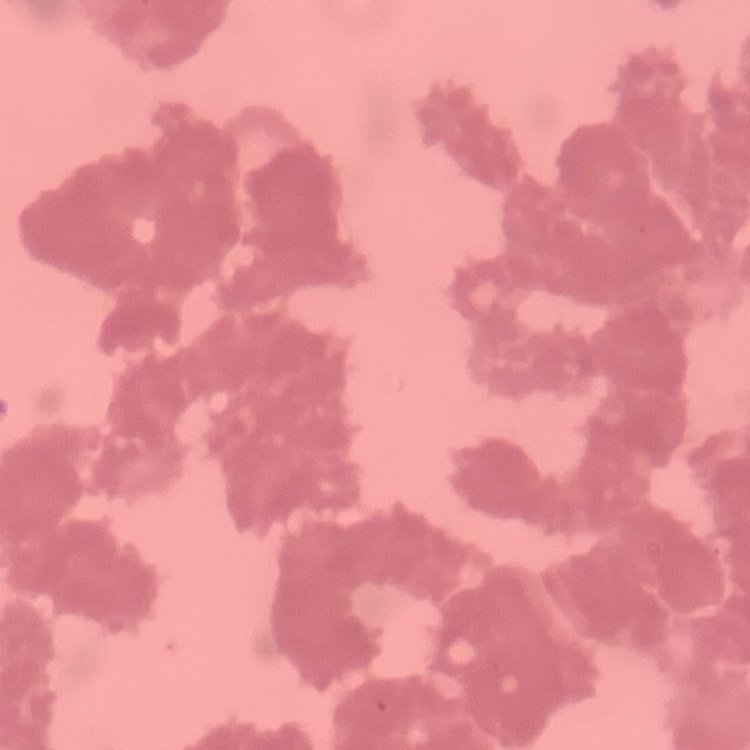

Summary:
  - Red blood cell morphology: rouleaux formation
  - Preparation: thin peripheral smear
  - Stain: Field's or Giemsa
  - Image type: one tile cut from a larger photomicrograph